Give the preparation type.
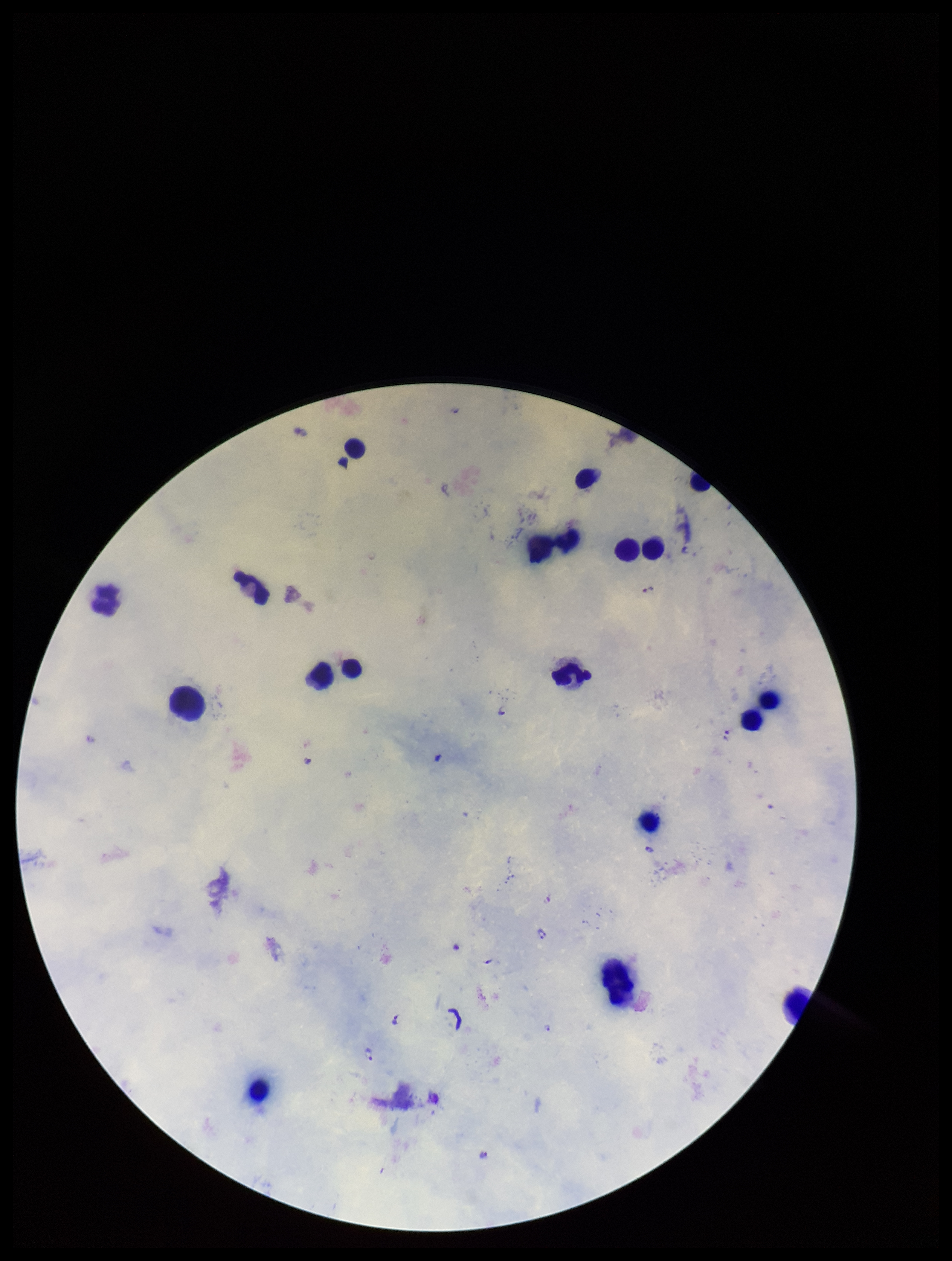

Thick.

Plasmodium parasites = detected
patient malaria status = positive
stain = Giemsa
parasite count = 9
capture = smartphone photograph through the microscope eyepiece
field of view = single
leukocyte count = 19
species reported for this patient = Plasmodium falciparum
image size = 952×1261 pixels